Classify this cell by malaria status.
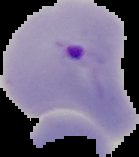

Parasitized.

Image is 139×157 pixels. Segmented cell region on a black background. From a thin blood film.